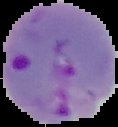

image size = 118×127 pixels
result = Plasmodium parasites detected
image type = segmented cell region on a black background
preparation = thin blood film